Name the cell type shown.
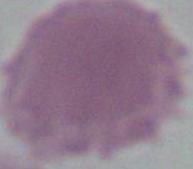
This is an erythrocyte.

Summary:
  - Magnification: 1000x
  - Modality: photomicrograph